Locate every blood parasite and identify its species.
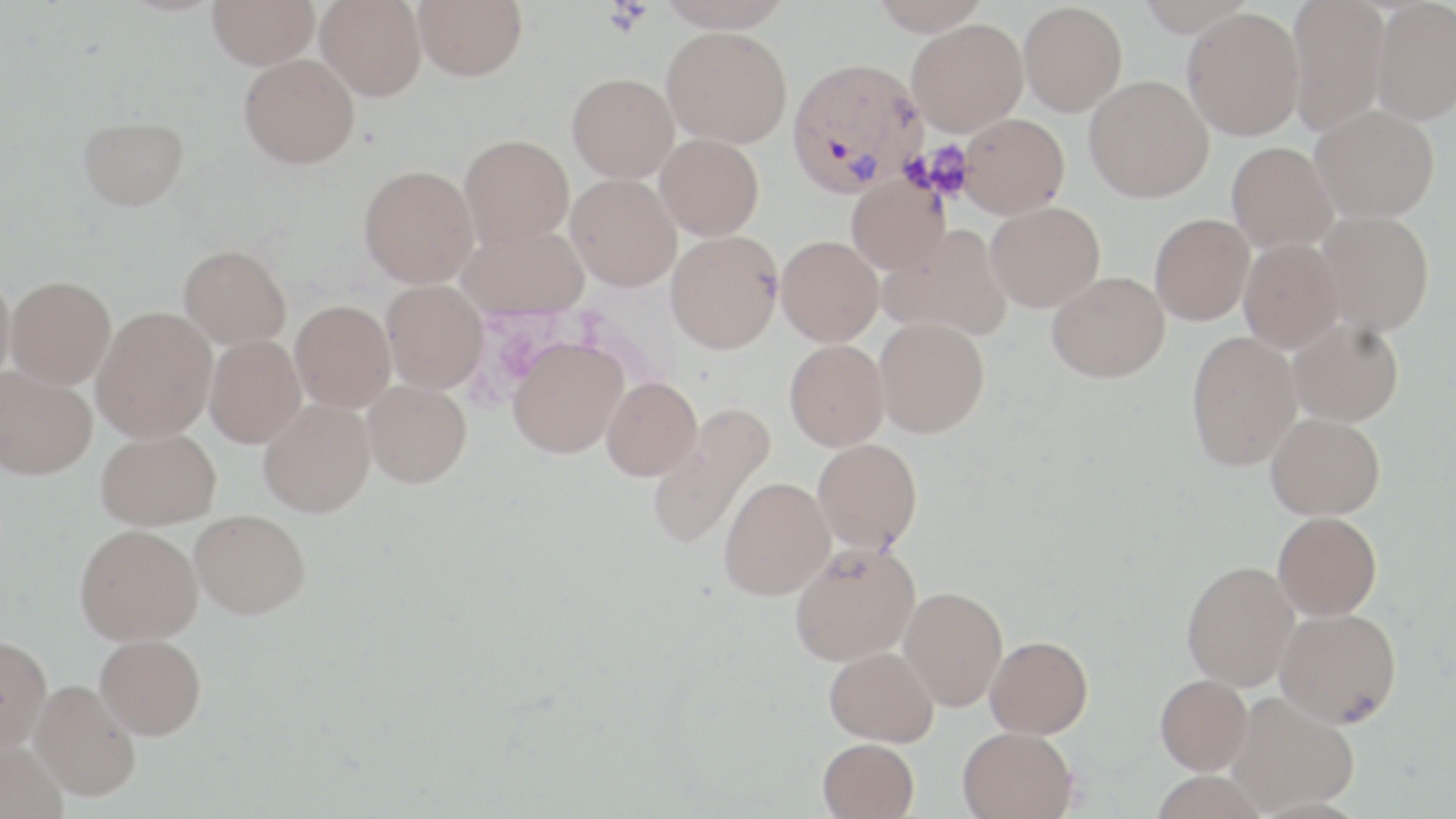

Approximate bounding boxes as (x1,y1)-(x2,y2) corner pairs in pixels.
Plasmodium vivax-infected red blood cells: (787,57)-(927,195).
No Plasmodium falciparum, Plasmodium ovale, Plasmodium malariae, Babesia divergens, or Trypanosoma brucei observed.

slide-level diagnosis = Plasmodium vivax
uninfected red blood cell locations = approximate bounding boxes as (x1,y1)-(x2,y2) corner pairs in pixels: (208,0)-(320,69), (316,0)-(426,101), (413,0)-(527,80), (656,0)-(794,32), (869,0)-(990,36), (1136,0)-(1256,37), (1287,0)-(1391,134), (1371,1)-(1456,124), (1018,2)-(1127,116), (1182,7)-(1305,140), (907,18)-(1028,135), (661,26)-(793,148), (239,54)-(359,169), (567,72)-(679,183), (1084,75)-(1214,203), (1310,104)-(1440,222), (959,113)-(1069,219), (78,116)-(189,211), (655,133)-(764,240), (459,134)-(574,249), (1226,142)-(1337,253), (358,165)-(478,288), (565,174)-(682,292), (847,175)-(950,274), (986,201)-(1105,312), (1316,210)-(1434,335), (1149,214)-(1254,325), (458,222)-(588,319), (879,225)-(1013,342), (665,230)-(783,353), (776,235)-(883,346), (1239,238)-(1344,353), (179,243)-(291,348), (0,269)-(15,389), (1047,271)-(1170,382), (6,276)-(116,388), (381,281)-(488,394), (290,300)-(396,413), (92,306)-(218,443), (874,317)-(990,437), (1287,318)-(1404,426), (1186,330)-(1302,471), (204,335)-(306,448), (507,337)-(628,458), (785,339)-(889,451), (0,366)-(97,479), (602,377)-(702,481), (362,380)-(471,487), (258,398)-(376,517), (647,402)-(775,551), (1266,412)-(1385,519), (95,428)-(221,529), (813,438)-(923,553), (719,477)-(835,600), (190,508)-(311,618), (1273,511)-(1382,621), (74,524)-(203,645), (789,541)-(920,666), (1182,560)-(1300,691), (898,586)-(1008,712), (1275,607)-(1402,728), (95,633)-(206,738), (0,635)-(52,752), (985,635)-(1093,738), (825,646)-(939,747), (1155,674)-(1252,775), (30,680)-(141,801), (1226,692)-(1360,814), (958,725)-(1077,819), (0,738)-(68,819), (818,738)-(919,819), (1149,770)-(1270,819)
image size = 1456×819 pixels
magnification = 1000x
stain = May-Grünwald-Giemsa
modality = light microscopy
platelet locations = approximate bounding boxes as (x1,y1)-(x2,y2) corner pairs in pixels: (604,1)-(651,36)
preparation = thin blood smear
field of view = one of a larger specimen